Locate every leukocyte (white blood cell).
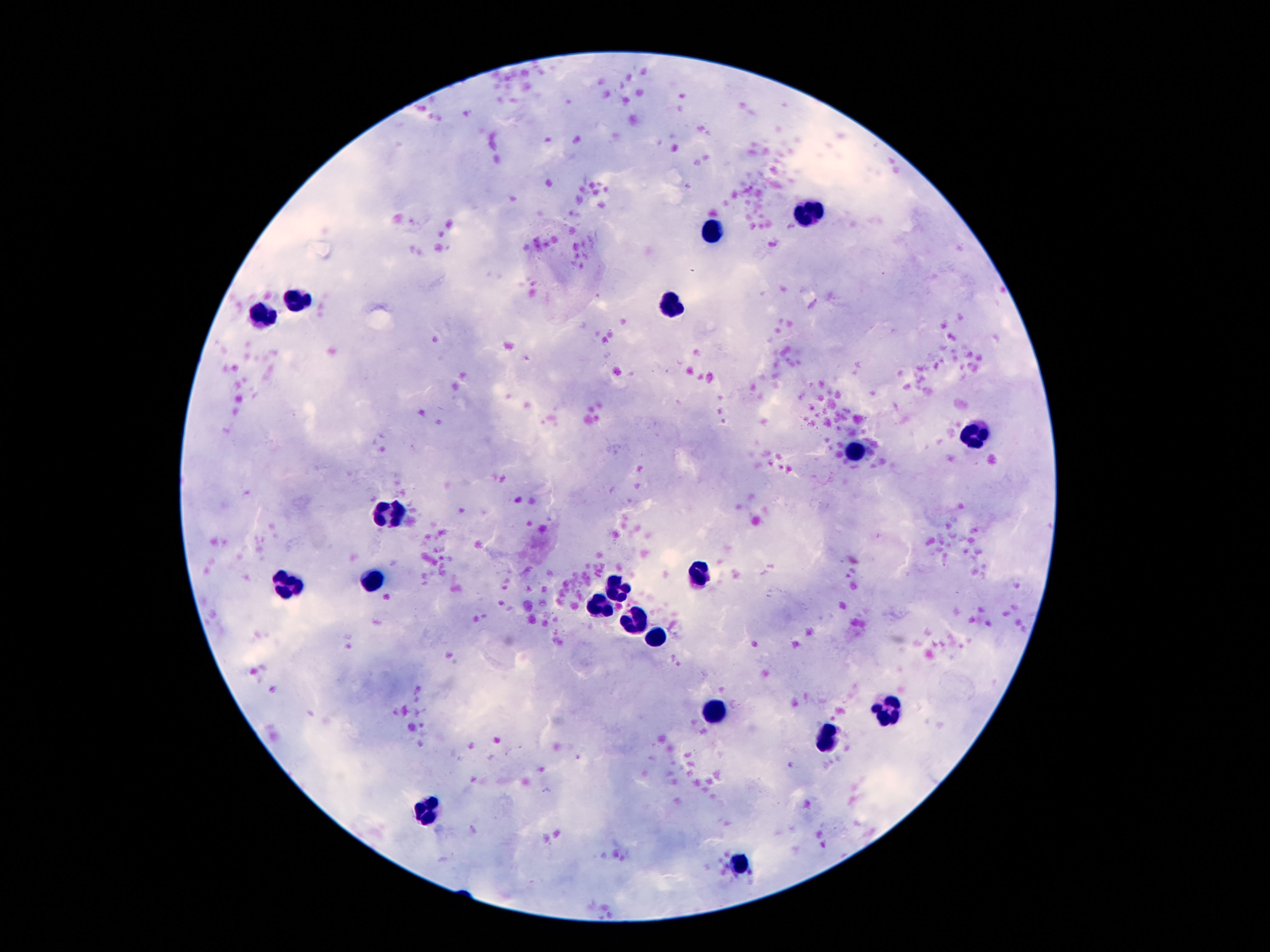

Approximate centers as {x, y} in pixels.
Leukocytes: {804, 214}, {715, 235}, {297, 300}, {670, 305}, {260, 313}, {974, 436}, {855, 451}, {387, 510}, {705, 574}, {379, 578}, {289, 588}, {617, 588}, {597, 611}, {636, 622}, {656, 635}, {713, 710}, {892, 712}, {826, 740}, {428, 809}, {742, 863}.

field_of_view: one from this slide
image_size: 1270×952 pixels
magnification: 100x
capture: smartphone camera through the microscope eyepiece
preparation: thick blood film
stain: Giemsa
patient_malaria_status: not infected